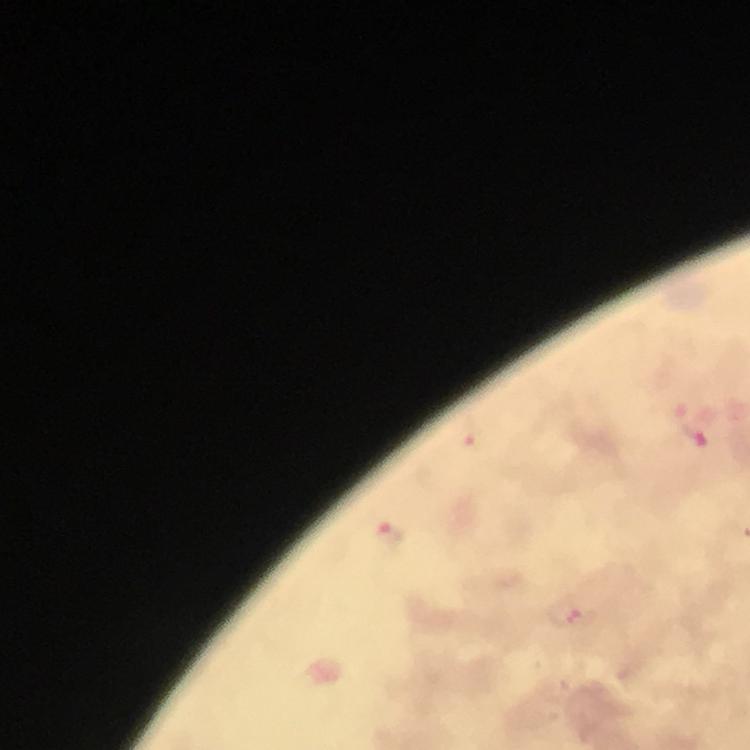

preparation = thick smear
context = from a malaria diagnostic workup
stain = Giemsa
magnification = 100x
cropped from = one field of view
Plasmodium parasite locations = approximate centers as {x, y} in pixels: {695, 435}, {477, 444}, {390, 536}, {583, 617}
capture = smartphone mounted on the microscope
image size = 750×750 pixels
immersion oil = applied